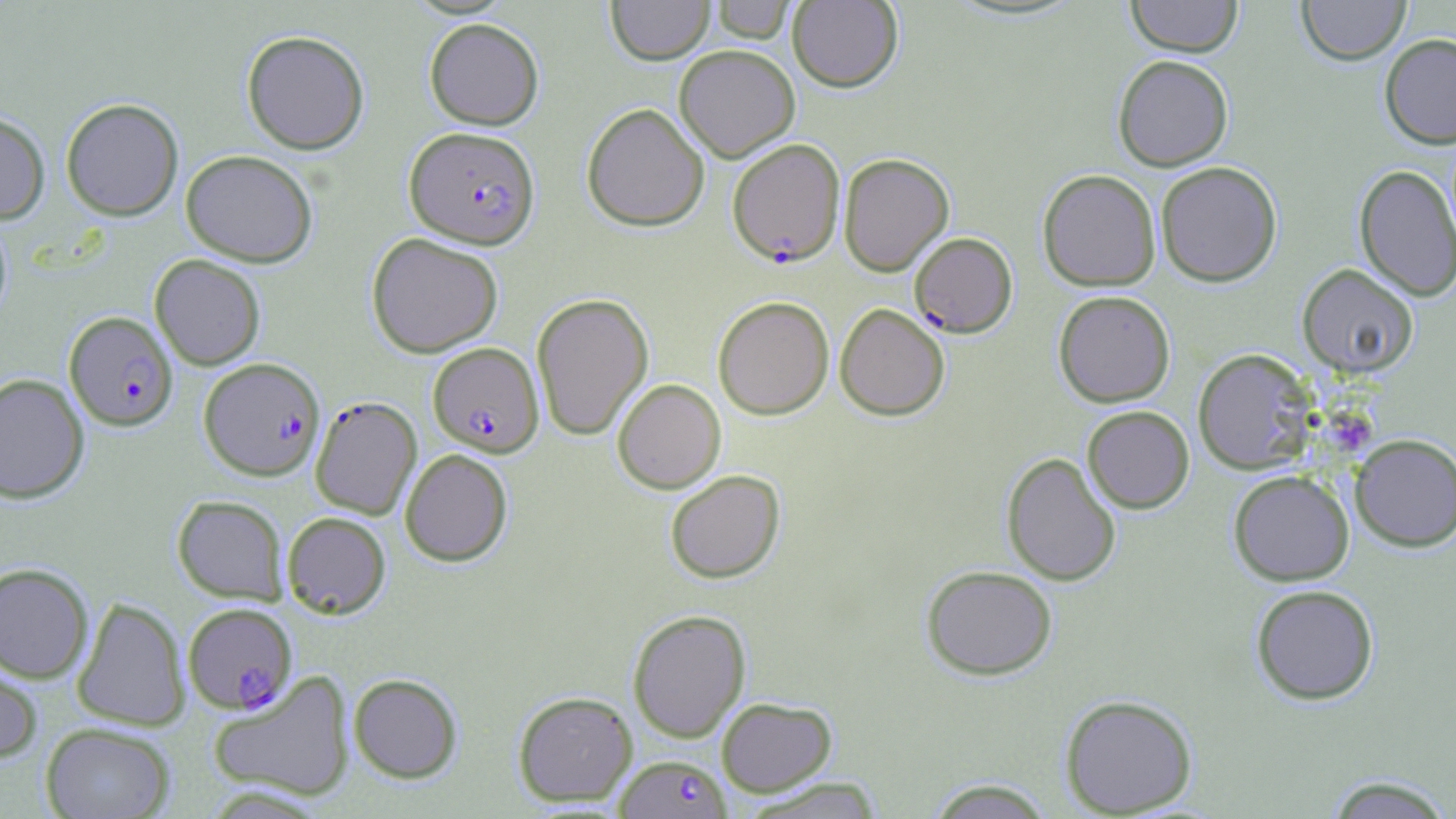

slide-level diagnosis = Plasmodium falciparum
preparation = thin blood film
image size = 1456×819 pixels
Plasmodium falciparum-infected red blood cell locations = approximate bounding boxes as named x1/y1/x2/y2 corners in pixels: (x1=404, y1=126, x2=540, y2=248), (x1=727, y1=138, x2=845, y2=267), (x1=909, y1=231, x2=1018, y2=337), (x1=64, y1=311, x2=178, y2=431), (x1=428, y1=342, x2=544, y2=456), (x1=199, y1=357, x2=326, y2=480), (x1=310, y1=396, x2=422, y2=519), (x1=183, y1=602, x2=297, y2=713), (x1=614, y1=754, x2=731, y2=819)
stain = May-Grünwald-Giemsa
uninfected red blood cell locations = approximate bounding boxes as named x1/y1/x2/y2 corners in pixels: (x1=606, y1=0, x2=714, y2=65), (x1=710, y1=0, x2=796, y2=43), (x1=787, y1=0, x2=903, y2=92), (x1=1125, y1=0, x2=1243, y2=57), (x1=1297, y1=0, x2=1410, y2=65), (x1=424, y1=18, x2=544, y2=130), (x1=241, y1=29, x2=370, y2=154), (x1=1379, y1=33, x2=1456, y2=148), (x1=673, y1=44, x2=800, y2=161), (x1=1112, y1=54, x2=1233, y2=171), (x1=60, y1=97, x2=184, y2=221), (x1=581, y1=102, x2=709, y2=231), (x1=0, y1=111, x2=50, y2=224), (x1=180, y1=149, x2=318, y2=267), (x1=838, y1=153, x2=954, y2=276), (x1=1155, y1=161, x2=1283, y2=286), (x1=1354, y1=163, x2=1456, y2=302), (x1=1037, y1=169, x2=1161, y2=291), (x1=0, y1=213, x2=13, y2=323), (x1=366, y1=232, x2=503, y2=358), (x1=150, y1=254, x2=266, y2=370), (x1=1297, y1=264, x2=1419, y2=378), (x1=1053, y1=290, x2=1175, y2=407), (x1=531, y1=292, x2=654, y2=441), (x1=713, y1=295, x2=834, y2=420), (x1=834, y1=303, x2=950, y2=421), (x1=1192, y1=348, x2=1316, y2=474), (x1=0, y1=373, x2=90, y2=503), (x1=612, y1=378, x2=726, y2=493), (x1=1082, y1=405, x2=1194, y2=513), (x1=1351, y1=433, x2=1456, y2=551), (x1=399, y1=449, x2=513, y2=566), (x1=1001, y1=452, x2=1122, y2=586), (x1=665, y1=469, x2=786, y2=583), (x1=1228, y1=470, x2=1354, y2=586), (x1=172, y1=495, x2=288, y2=603), (x1=282, y1=511, x2=391, y2=618), (x1=0, y1=562, x2=94, y2=683), (x1=920, y1=564, x2=1058, y2=680), (x1=1250, y1=584, x2=1379, y2=705), (x1=72, y1=596, x2=190, y2=731), (x1=627, y1=608, x2=751, y2=742), (x1=0, y1=650, x2=43, y2=764), (x1=207, y1=671, x2=356, y2=802), (x1=348, y1=673, x2=463, y2=783), (x1=512, y1=690, x2=637, y2=806), (x1=1059, y1=694, x2=1198, y2=816), (x1=716, y1=697, x2=837, y2=796), (x1=40, y1=723, x2=175, y2=819), (x1=1321, y1=774, x2=1455, y2=817), (x1=741, y1=776, x2=887, y2=817), (x1=925, y1=777, x2=1055, y2=818)
modality = light microscopy
magnification = 1000x
field of view = single
platelet locations = approximate bounding boxes as named x1/y1/x2/y2 corners in pixels: (x1=1326, y1=413, x2=1378, y2=462)